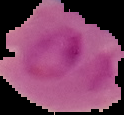
Summary:
  - Preparation: thin blood film
  - Image size: 124×115 pixels
  - Malaria status: parasitized
  - Image type: segmented cell region with the area outside set to black